Draw a bounding box around every Plasmodium parasite.
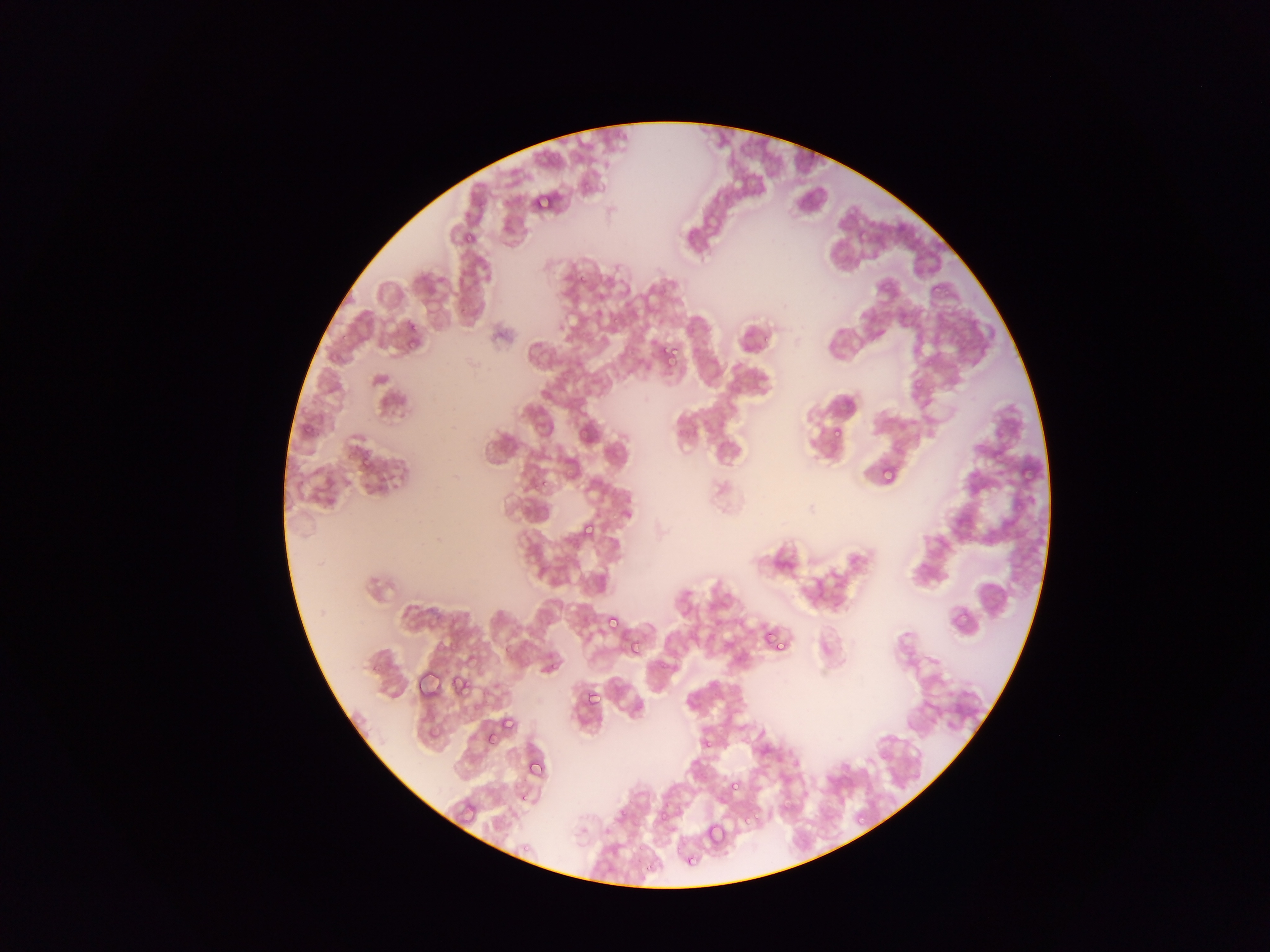
Approximate bounding boxes as {left, top, right, bottom} in pixels.
Plasmodium parasites: {530, 191, 553, 212}, {464, 235, 473, 243}, {927, 281, 946, 300}, {405, 320, 420, 336}, {685, 321, 701, 338}, {404, 330, 422, 352}, {665, 342, 682, 360}, {910, 375, 926, 394}, {576, 419, 600, 446}, {299, 423, 314, 437}, {832, 426, 843, 437}, {991, 444, 1009, 463}, {353, 448, 376, 473}, {1019, 460, 1039, 483}, {878, 463, 896, 483}, {540, 478, 554, 490}, {578, 519, 599, 544}, {950, 605, 975, 634}, {603, 612, 623, 634}, {758, 624, 791, 657}, {628, 637, 646, 657}, {500, 639, 517, 658}, {413, 672, 441, 702}, {452, 674, 474, 697}, {580, 687, 601, 710}, {498, 713, 520, 737}, {488, 735, 494, 746}, {702, 740, 716, 750}, {524, 755, 549, 783}, {725, 776, 743, 796}, {777, 800, 794, 817}, {653, 806, 676, 830}, {855, 810, 869, 825}, {703, 821, 728, 850}, {681, 848, 701, 870}.

Single field of view. Photographed through a microscope with a mobile-phone camera. Image is 1270×952 pixels. Thin blood smear. Collected in Ghana.